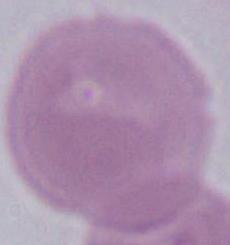
An erythrocyte is seen. Micrograph. 1000x magnification.